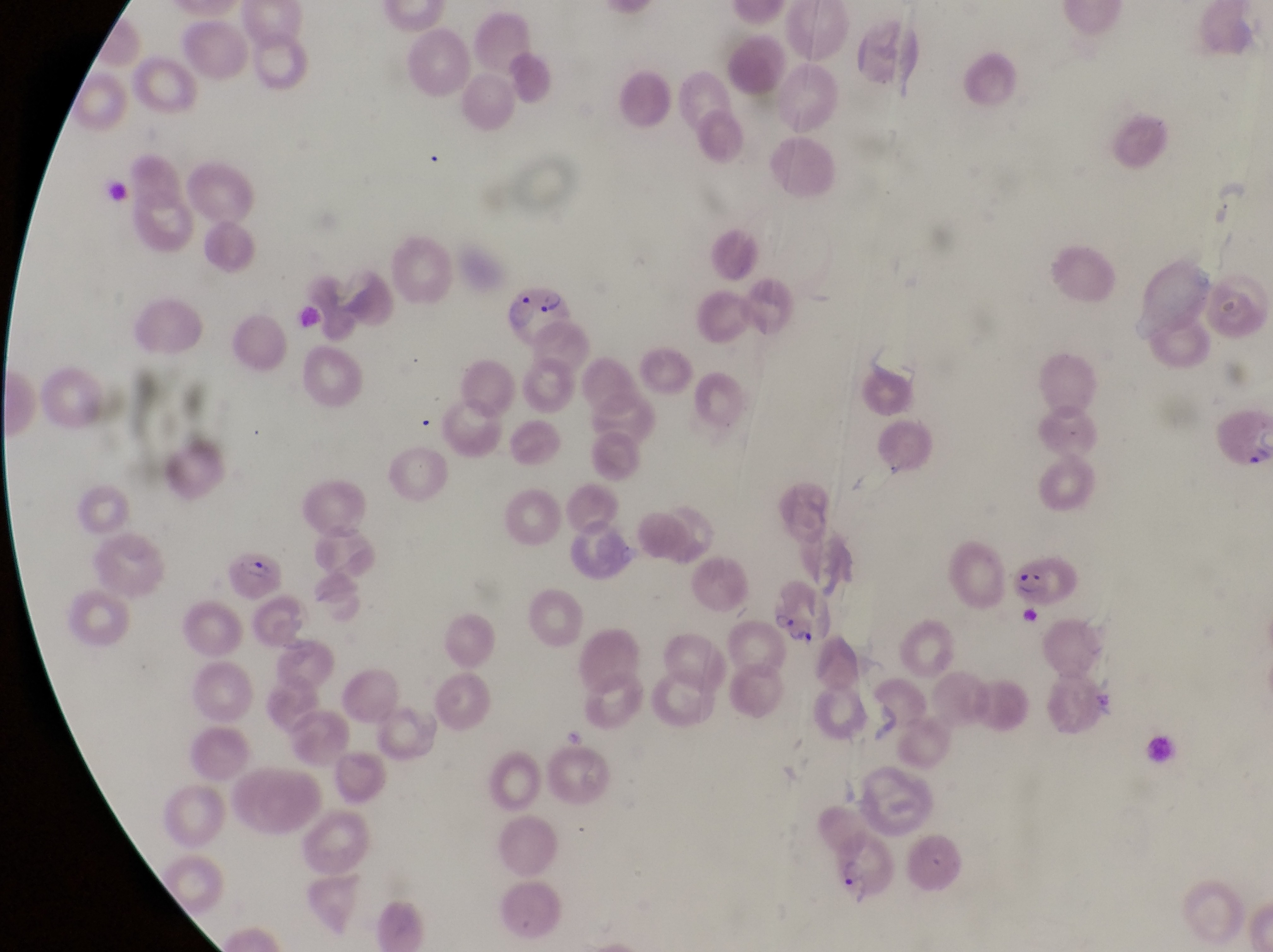
Approximate bounding boxes as left top right bottom in pixels. Parasitised red blood cell locations: 491 280 579 358; 1013 542 1076 609; 224 550 287 600; 768 579 837 654; 831 831 896 908. Thin blood film. Sample from Uganda. Magnification of 1000x. Captured by a smartphone held over the eyepiece of an Olympus CX-23 microscope. Single field of view. Image is 1273×952 pixels.